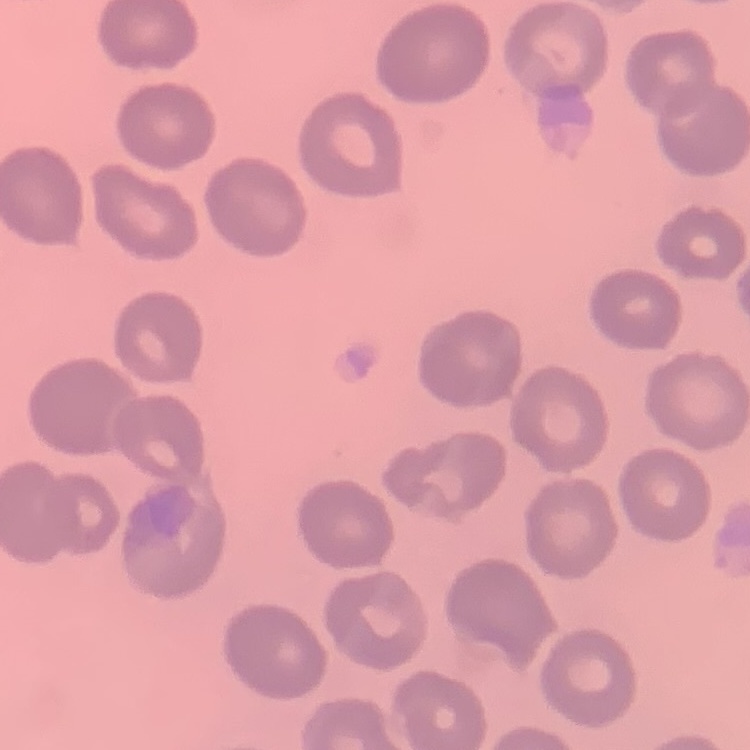

Summary:
  - Red blood cell morphology: no rouleaux formation
  - Stain: Field's or Giemsa
  - Preparation: thin blood film
  - Image type: square crop of a larger photomicrograph